Identify the parasite.
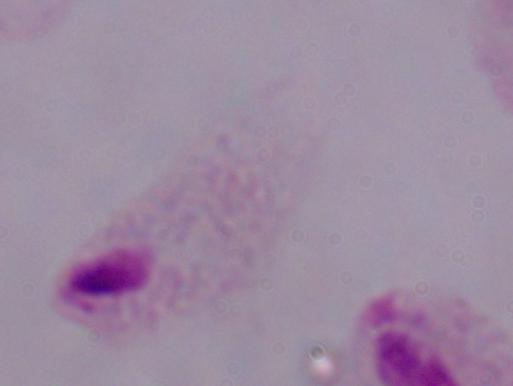

This is a trichomonad.

Summary:
  - Magnification: 1000x
  - Modality: micrograph